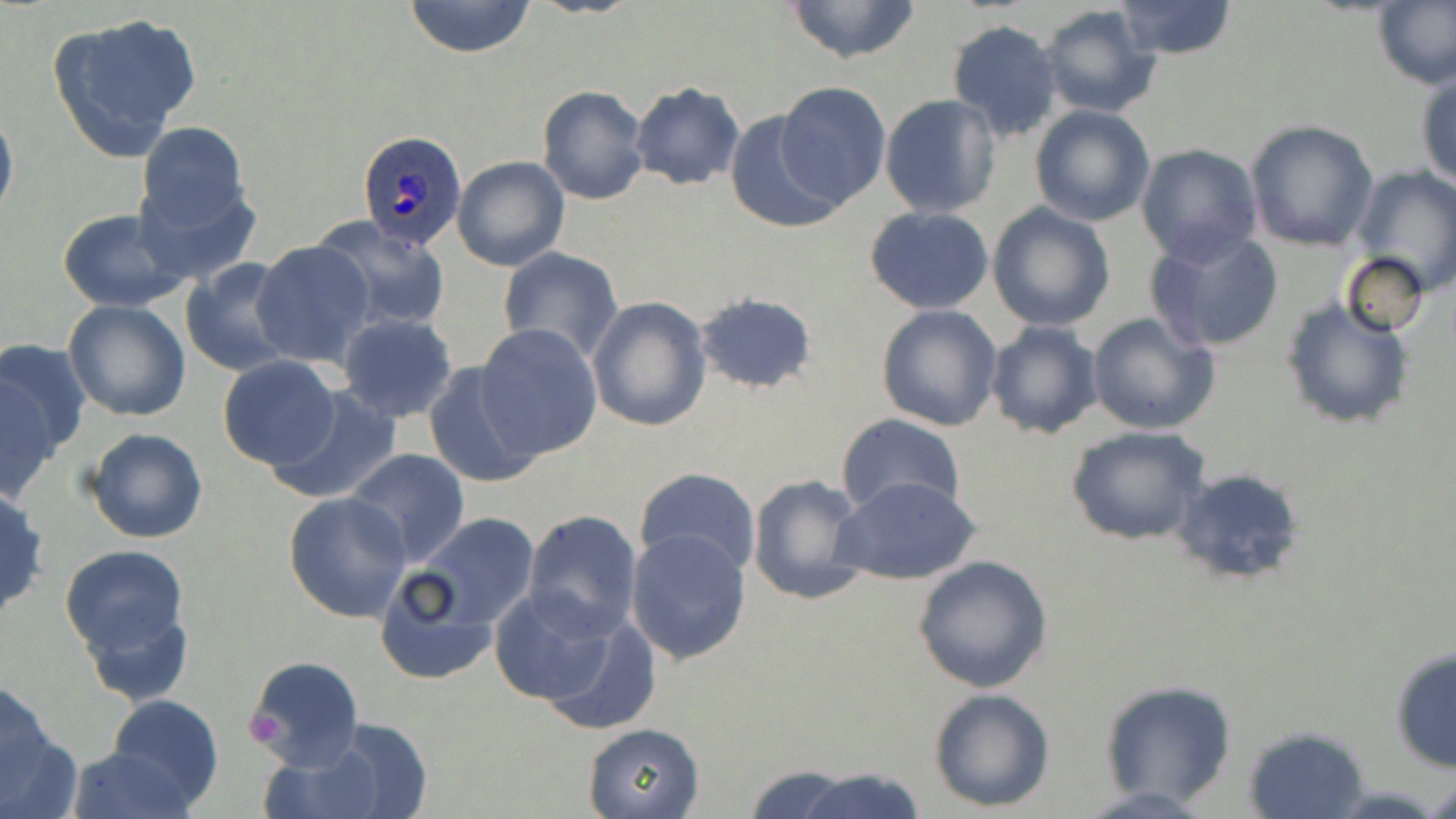
slide-level diagnosis = Plasmodium ovale
platelet locations = approximate bounding boxes as (x1,y1)-(x2,y2) corner pairs in pixels: (245,709)-(287,744)
magnification = 1000x
Plasmodium ovale-infected red blood cell locations = approximate bounding boxes as (x1,y1)-(x2,y2) corner pairs in pixels: (355,129)-(468,253)
modality = light microscopy
preparation = thin blood smear
image size = 1456×819 pixels
field of view = one of a larger specimen
uninfected red blood cell locations = approximate bounding boxes as (x1,y1)-(x2,y2) corner pairs in pixels: (402,0)-(536,57), (780,0)-(926,66), (1113,0)-(1239,61), (1373,1)-(1456,91), (1038,4)-(1162,117), (47,11)-(203,163), (946,20)-(1063,142), (1416,68)-(1456,190), (775,81)-(891,207), (628,82)-(744,191), (537,85)-(649,205), (879,94)-(1002,219), (0,105)-(18,229), (1028,105)-(1156,227), (722,111)-(847,232), (134,120)-(254,246), (1245,120)-(1379,251), (1134,144)-(1262,266), (452,155)-(570,272), (1352,165)-(1456,296), (987,201)-(1116,333), (863,207)-(995,315), (57,208)-(190,311), (316,220)-(450,330), (1145,228)-(1284,354), (252,239)-(375,367), (498,246)-(623,365), (1340,252)-(1430,338), (180,259)-(299,378), (693,289)-(818,395), (587,296)-(711,433), (1278,297)-(1414,433), (62,299)-(191,422), (875,304)-(1004,431), (1087,310)-(1220,437), (336,312)-(458,422), (984,321)-(1103,439), (472,324)-(603,459), (0,338)-(88,491), (217,356)-(341,470), (420,362)-(543,488), (265,383)-(403,506), (835,414)-(966,521), (1064,424)-(1214,547), (83,426)-(209,544), (345,448)-(470,567), (633,466)-(762,578), (1168,466)-(1309,587), (747,472)-(871,606), (834,475)-(983,589), (0,483)-(50,624), (284,492)-(412,623), (521,509)-(643,637), (408,512)-(542,635), (624,528)-(752,666), (60,544)-(190,675), (912,554)-(1054,692), (374,558)-(514,685), (489,585)-(628,712), (538,607)-(663,736), (1389,645)-(1455,774), (245,653)-(363,770), (1098,679)-(1238,807), (0,685)-(79,819), (928,687)-(1056,812), (105,692)-(225,810), (299,719)-(435,819), (583,723)-(705,818), (1241,724)-(1372,819), (253,740)-(391,819), (65,745)-(197,819), (744,764)-(868,818), (791,766)-(926,819), (1426,777)-(1456,819), (1070,784)-(1223,818)
stain = May-Grünwald-Giemsa